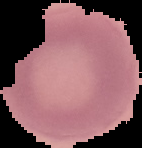
Summary:
  - Image type: segmented cell region on a black background
  - Result: negative for malaria parasites
  - Image size: 142×148 pixels
  - Preparation: thin blood smear